Report the malaria status of this cell.
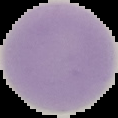

Uninfected.

Summary:
  - Image size: 118×118 pixels
  - Image type: cell region segmented out of the field of view; surrounding area masked to black
  - Preparation: thin blood smear